Assess this cell for malaria.
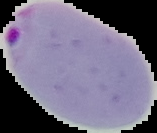

Parasitized.

Summary:
  - Preparation: thin blood film
  - Image type: segmented cell region with the area outside set to black
  - Image size: 157×133 pixels